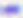
Summary:
  - Magnification: 400x
  - Modality: photomicrograph
  - Identification: Toxoplasma gondii